Locate every Plasmodium malariae-infected red blood cell.
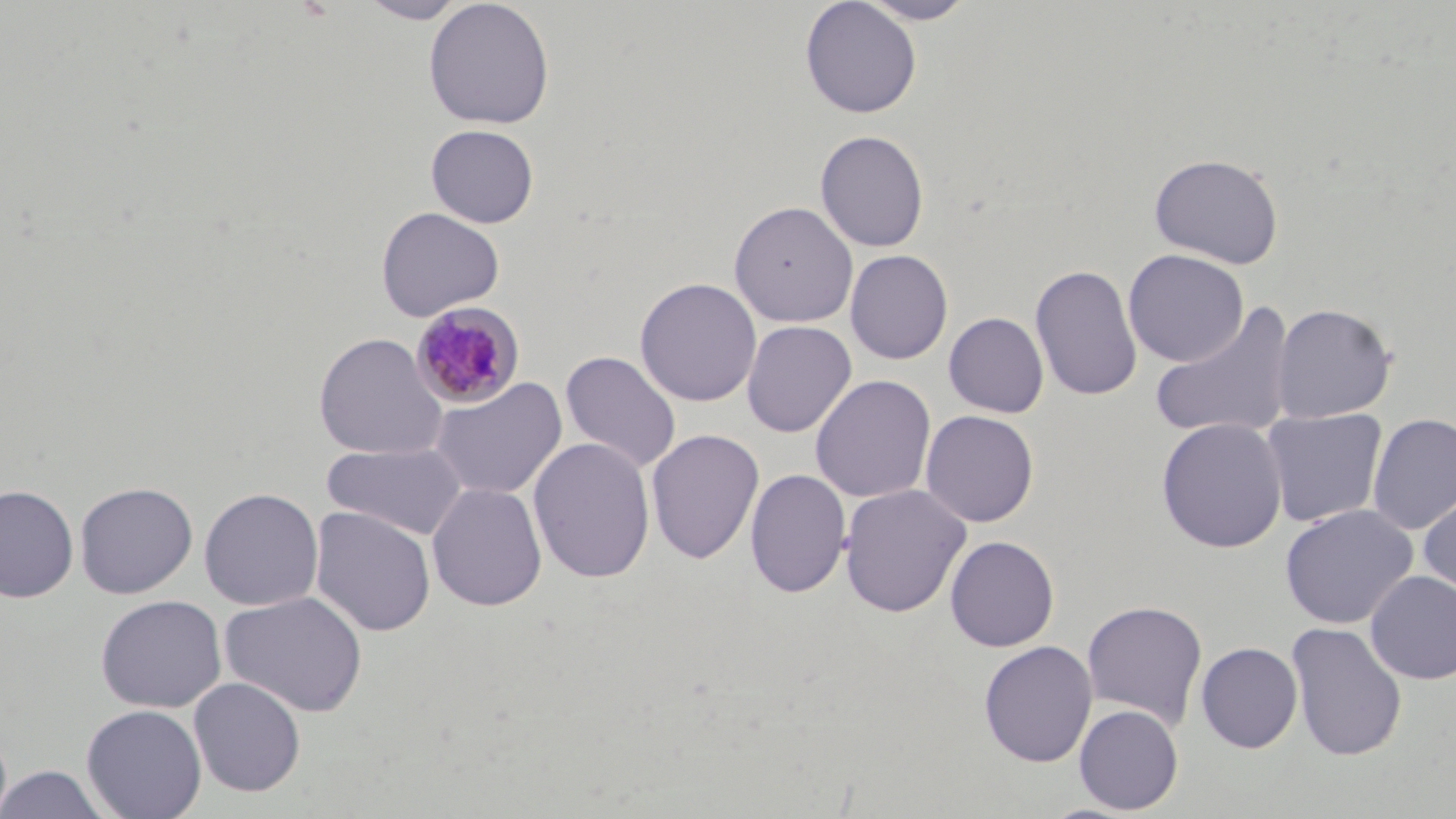
Approximate bounding boxes as [x1, y1, x2, y2] in pixels.
Plasmodium malariae-infected red blood cells: [408, 301, 524, 411].

slide-level diagnosis = Plasmodium malariae
modality = light microscopy
uninfected red blood cell locations = approximate bounding boxes as [x1, y1, x2, y2] in pixels: [358, 0, 470, 24], [799, 0, 922, 119], [857, 0, 978, 25], [422, 1, 555, 130], [425, 124, 540, 228], [815, 129, 930, 252], [1148, 153, 1284, 269], [729, 201, 858, 328], [376, 206, 505, 322], [1122, 248, 1249, 367], [844, 249, 953, 364], [1029, 264, 1143, 403], [634, 277, 762, 407], [1150, 302, 1297, 441], [1270, 303, 1397, 424], [943, 312, 1049, 418], [741, 320, 857, 438], [312, 332, 448, 460], [559, 350, 682, 473], [810, 374, 936, 504], [429, 377, 568, 501], [1260, 408, 1388, 527], [920, 409, 1039, 527], [1367, 413, 1456, 535], [1156, 418, 1288, 553], [645, 429, 765, 565], [528, 437, 656, 584], [320, 441, 469, 541], [745, 468, 851, 599], [74, 481, 198, 599], [427, 482, 548, 612], [0, 484, 79, 603], [838, 484, 972, 618], [198, 487, 324, 612], [1418, 489, 1456, 604], [1279, 504, 1418, 629], [310, 506, 436, 637], [945, 535, 1059, 652], [1365, 570, 1456, 684], [219, 590, 368, 718], [95, 594, 227, 713], [1081, 599, 1208, 730], [1286, 621, 1407, 762], [978, 640, 1098, 767], [1196, 642, 1303, 753], [188, 677, 306, 797], [81, 704, 207, 819], [1073, 704, 1184, 815], [0, 765, 113, 818]
magnification = 1000x
image size = 1456×819 pixels
field of view = one of a larger specimen
stain = May-Grünwald-Giemsa
preparation = thin blood smear